Outline each Plasmodium falciparum-infected red blood cell.
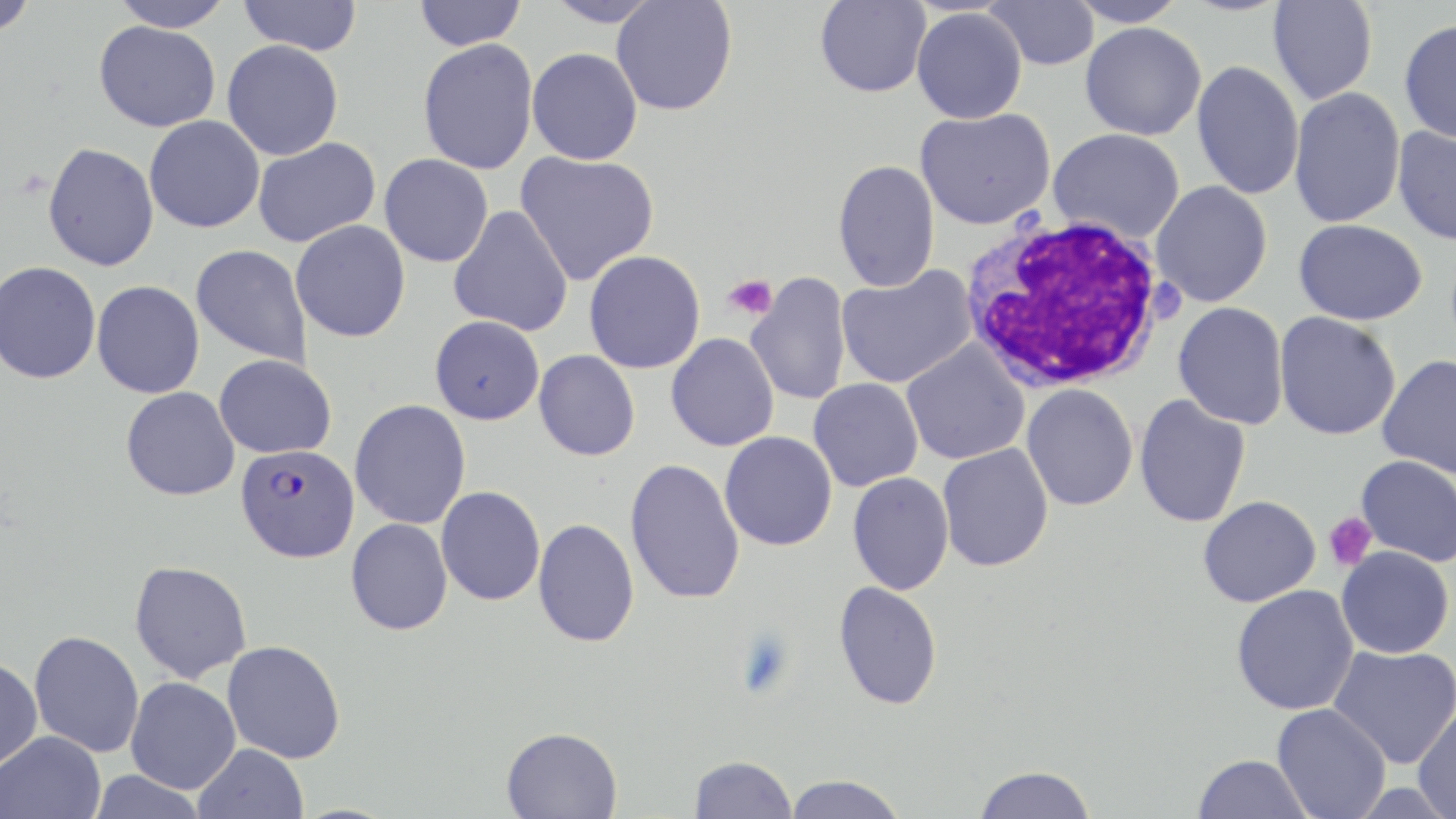

Approximate bounding boxes as (x1,y1)-(x2,y2) corner pairs in pixels.
Plasmodium falciparum-infected red blood cells: (236,443)-(360,562).

slide-level diagnosis = Plasmodium falciparum
uninfected red blood cell locations = approximate bounding boxes as (x1,y1)-(x2,y2) corner pairs in pixels: (0,0)-(39,37), (107,0)-(235,32), (237,0)-(363,55), (413,0)-(526,51), (544,0)-(664,28), (610,0)-(738,116), (983,0)-(1100,71), (1066,0)-(1189,28), (814,1)-(932,98), (1268,1)-(1377,106), (912,7)-(1027,124), (93,20)-(221,131), (1399,20)-(1456,144), (1080,22)-(1206,140), (418,38)-(538,175), (222,40)-(344,160), (527,48)-(643,165), (1191,61)-(1305,200), (1288,87)-(1406,229), (915,108)-(1055,230), (144,115)-(265,233), (1392,125)-(1456,245), (1049,128)-(1185,243), (253,137)-(381,248), (42,142)-(159,271), (515,151)-(660,286), (379,154)-(494,267), (832,160)-(940,293), (1150,181)-(1272,307), (448,205)-(574,336), (1293,219)-(1427,325), (290,220)-(411,342), (191,244)-(312,368), (584,250)-(705,374), (0,261)-(101,384), (836,264)-(977,389), (746,274)-(852,406), (92,281)-(205,399), (1173,302)-(1289,430), (1274,312)-(1401,441), (430,315)-(545,425), (666,333)-(779,451), (901,341)-(1030,466), (534,350)-(640,461), (214,354)-(337,458), (1377,355)-(1456,479), (808,378)-(924,491), (1021,384)-(1138,511), (121,386)-(240,500), (1134,394)-(1251,528), (349,399)-(471,529), (720,431)-(837,551), (937,443)-(1053,572), (1356,455)-(1456,567), (624,459)-(745,605), (847,471)-(954,595), (436,486)-(545,606), (1198,495)-(1321,607), (345,518)-(453,636), (532,518)-(640,648), (1335,545)-(1454,659), (129,560)-(252,683), (833,581)-(943,710), (1231,585)-(1359,715), (29,631)-(144,758), (222,640)-(346,764), (1327,645)-(1456,768), (0,657)-(43,771), (125,677)-(241,794), (1272,703)-(1391,819), (1412,703)-(1456,819), (500,726)-(623,819), (0,730)-(106,819), (193,744)-(309,818), (1193,754)-(1312,818), (689,755)-(797,818), (973,765)-(1096,819), (86,770)-(208,819), (783,774)-(908,819)
field of view = single
platelet locations = approximate bounding boxes as (x1,y1)-(x2,y2) corner pairs in pixels: (722,274)-(777,321), (1324,512)-(1377,571)
stain = May-Grünwald-Giemsa
preparation = thin blood film
magnification = 1000x
white blood cell locations = approximate bounding boxes as (x1,y1)-(x2,y2) corner pairs in pixels: (956,213)-(1171,394)
image size = 1456×819 pixels
modality = light microscopy